State the preparation type.
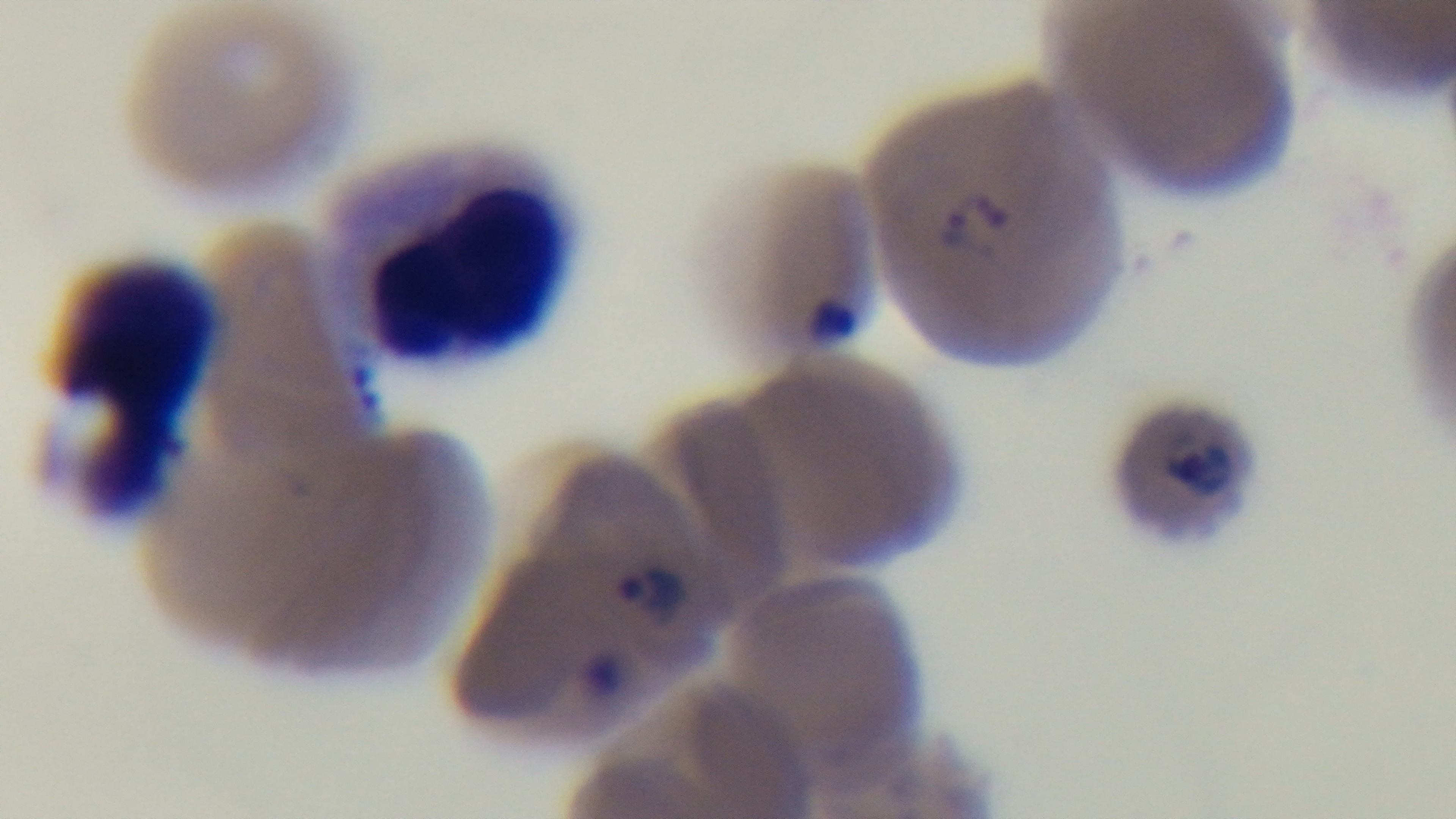

Thin.

Malaria status: positive. Oil-immersion objective, 100x. Single field of view. Giemsa stain. Light microscopy. Captured with a mounted 4K digital camera.